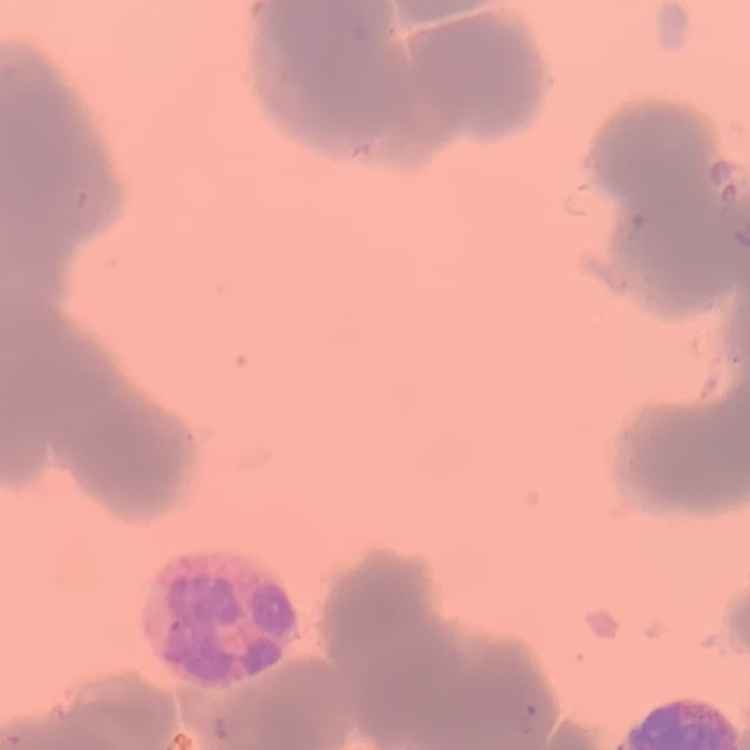 The red blood cells show rouleaux formation. One tile cut from a larger photomicrograph. Thin peripheral smear. Field's or Giemsa stain.